Describe the morphology of the red blood cells.
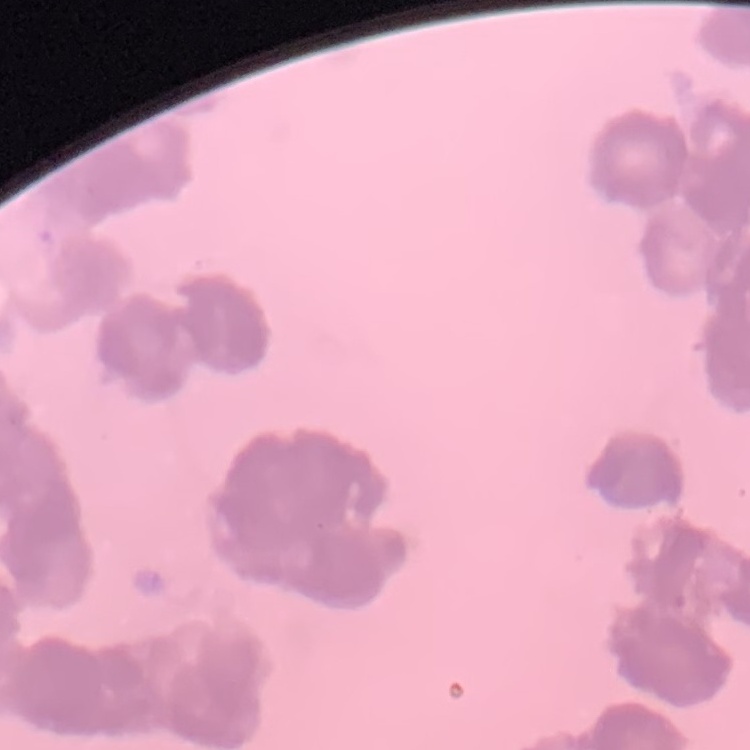
They show rouleaux formation.

stain = Field's or Giemsa
image type = square crop of a larger photomicrograph
preparation = thin blood smear